Point out Plasmodium parasites and leukocytes.
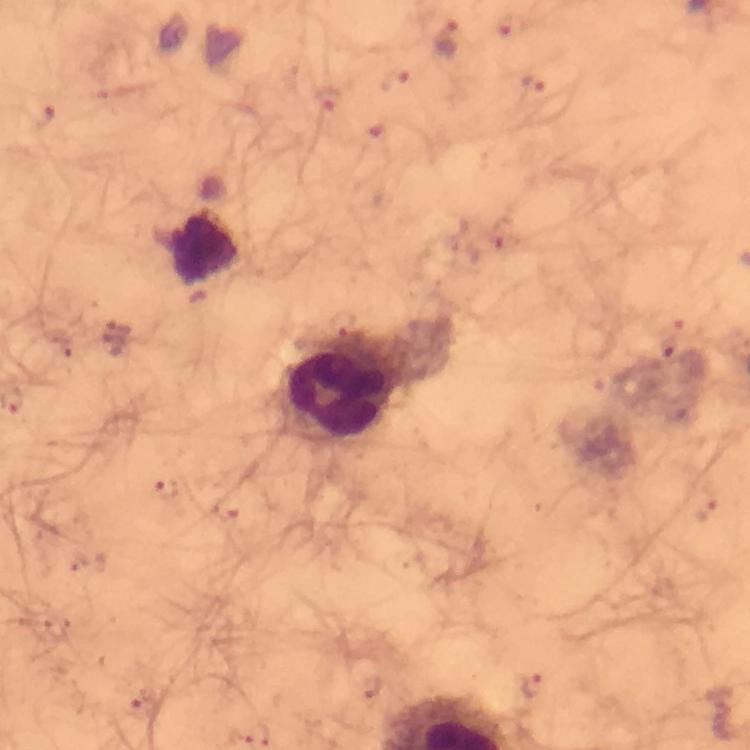
Approximate centers as {x, y} in pixels.
Plasmodium parasites: {513, 24}, {448, 37}, {398, 79}, {534, 83}, {326, 99}, {42, 115}, {504, 233}, {668, 346}, {167, 488}, {707, 507}, {532, 687}, {371, 688}, {142, 705}, {238, 736}.
Leukocytes: {340, 390}.

image size = 750×750 pixels
cropped from = one field of view
context = from a diagnostic examination for malaria
magnification = 100x
immersion oil = applied
preparation = thick blood film
stain = Giemsa
capture = smartphone photograph through a microscope